Identify the cell.
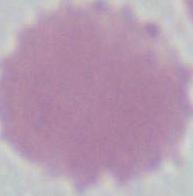
This is an erythrocyte.

magnification = 1000x
modality = photomicrograph